Comment on the morphology of the erythrocytes.
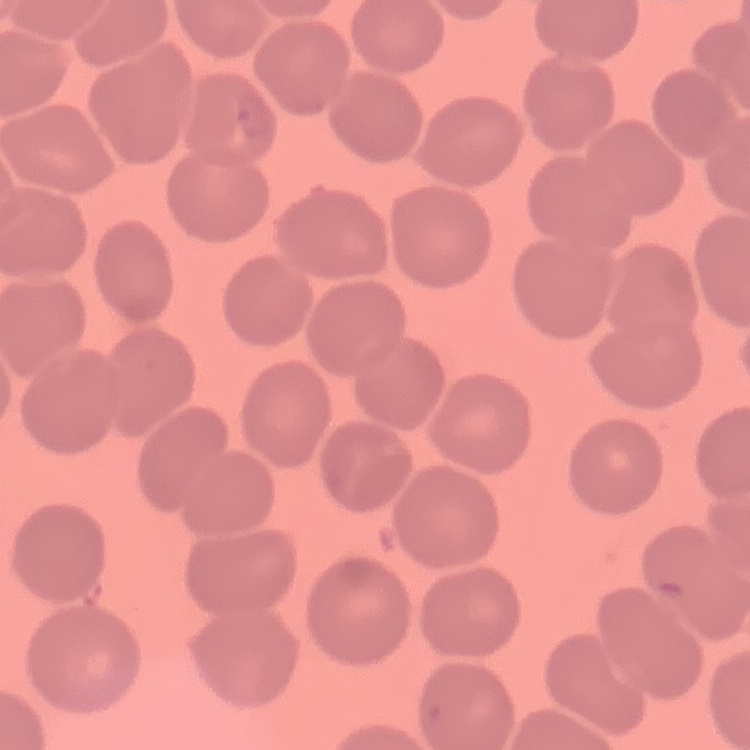
They show no rouleaux formation.

image_type: one tile cut from a larger photomicrograph
stain: Field's or Giemsa
preparation: thin blood smear